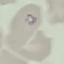
malaria_status: parasitized
image_type: automatically extracted cell patch, resized to 64 × 64 pixels
preparation: thin smear
stain: Giemsa
capture: smartphone through the microscope eyepiece